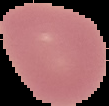 Segmented cell region on a black background. Image is 109×106 pixels. Malaria status: uninfected. From a thin blood smear.